Report the malaria status.
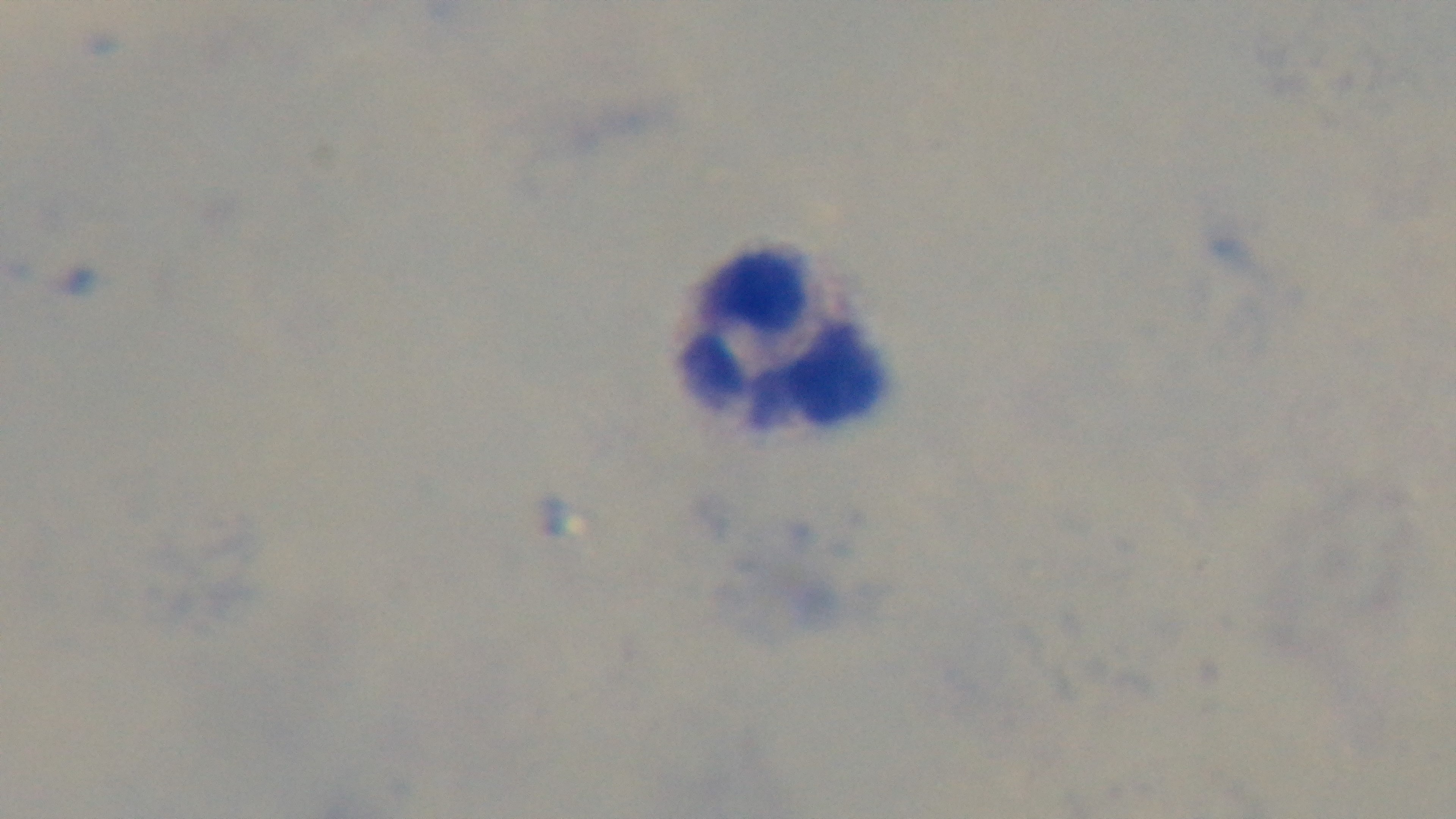

It is uninfected.

Summary:
  - Modality: light microscopy
  - Preparation: thick smear
  - Stain: Giemsa
  - Field of view: one from the slide
  - Capture: mounted 4K digital camera
  - Objective: 100x oil immersion